Give the position of each Plasmodium falciparum parasite with its life-cycle stage, each leukocyte, and any debris.
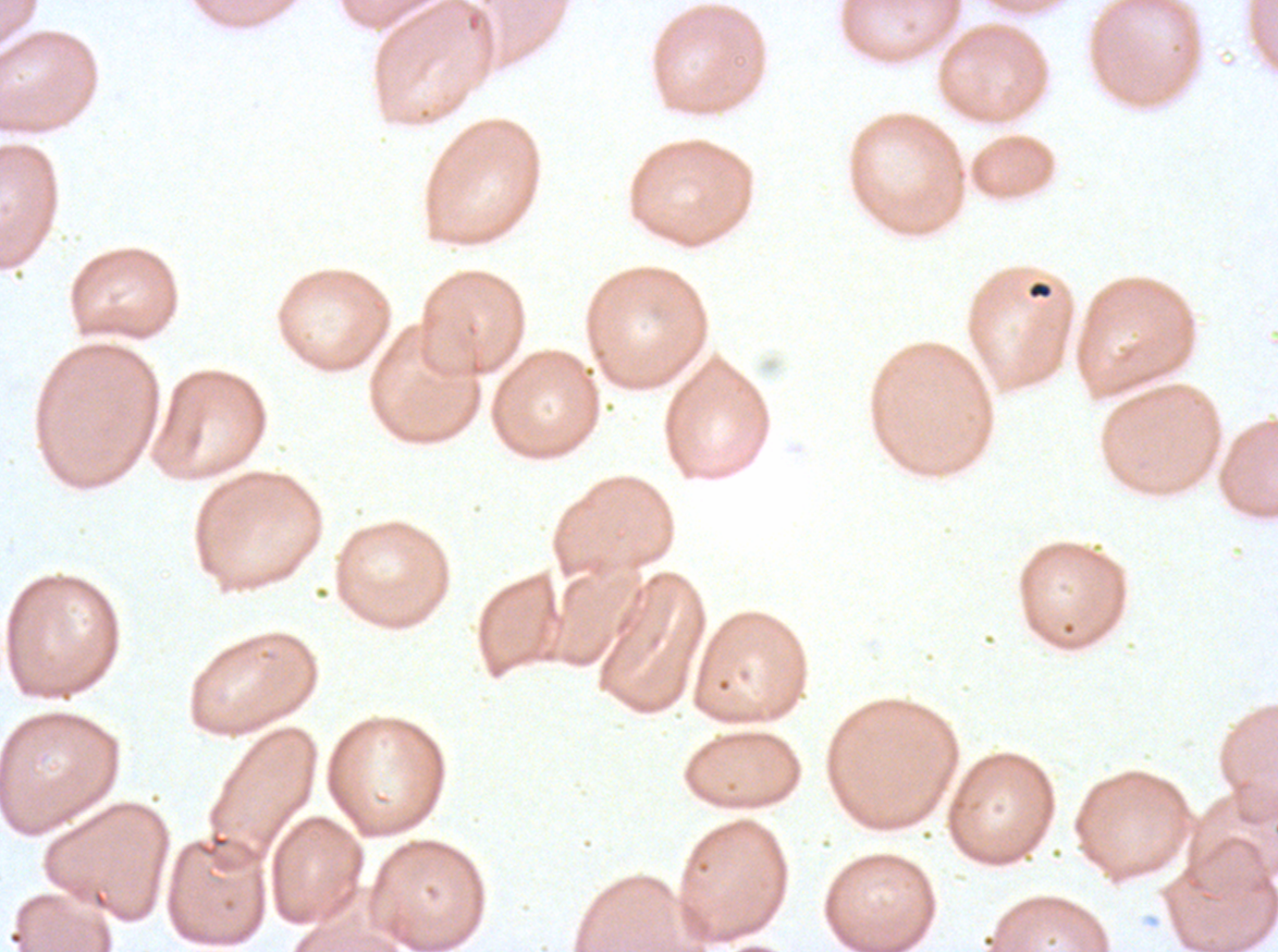

Approximate bounding rectangles given as corner coordinates in pixels from the top-left.
Debris: (x1=1026, y1=280, x2=1053, y2=299).
No rings, late-ring/early-trophozoite forms, mid trophozoites, late trophozoites, early schizonts, late schizonts, segmenters, gametocytes, or leukocytes observed.

field of view = sub-image separated from a larger composite
stain = Giemsa
specimen = Plasmodium falciparum from a patient in The Gambia, cultured ex vivo for 24 to 48 hours
image size = 1278×952 pixels
preparation = thin blood smear